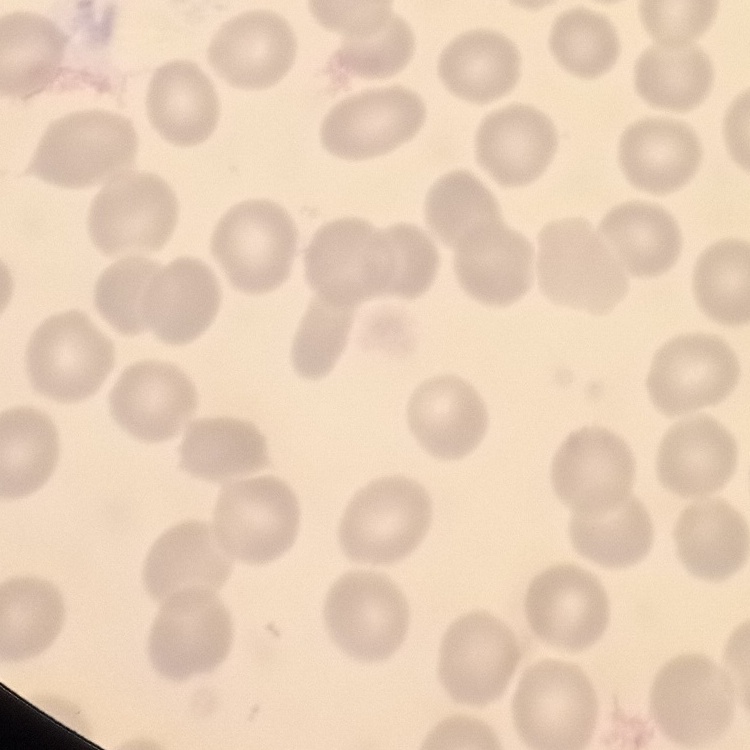
The erythrocytes show no rouleaux formation. Thin peripheral smear. Square crop of a larger photomicrograph. Field's or Giemsa stain.